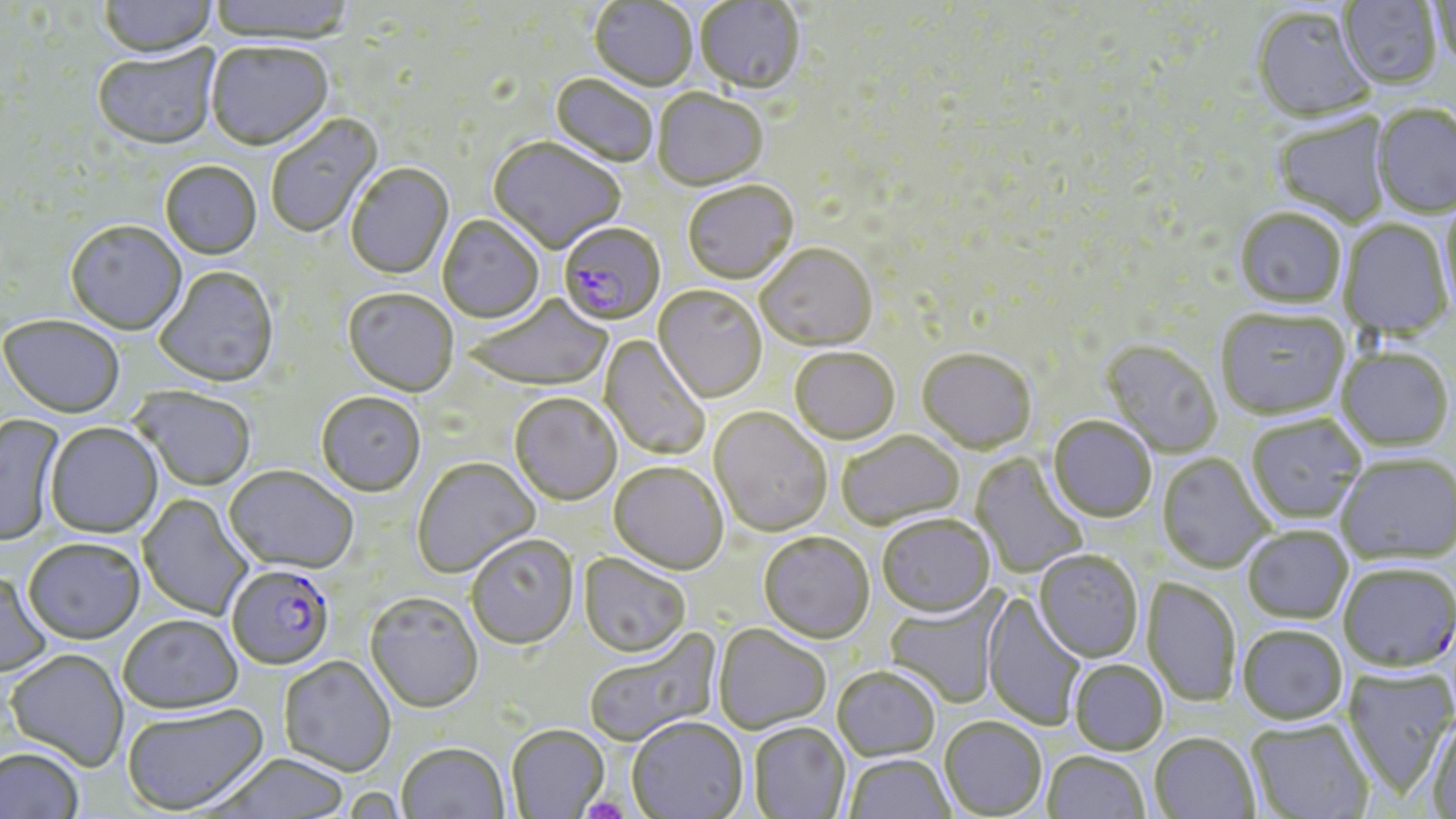
Summary:
  - Coordinate format: approximate bounding boxes as (x1, y1, x2, y2) in pixels
  - Platelet locations: (580, 797, 630, 819)
  - Plasmodium falciparum-infected red blood cell locations: (558, 224, 666, 328), (227, 567, 334, 671)
  - Uninfected red blood cell locations: (97, 0, 218, 61), (209, 0, 355, 46), (1427, 0, 1456, 75), (589, 1, 697, 92), (694, 1, 805, 97), (1338, 1, 1443, 90), (1251, 8, 1375, 125), (206, 44, 333, 153), (92, 46, 221, 152), (549, 75, 658, 169), (653, 91, 769, 192), (1371, 103, 1456, 217), (266, 113, 384, 240), (1272, 113, 1392, 227), (488, 138, 626, 256), (160, 162, 262, 262), (346, 164, 454, 280), (682, 182, 799, 288), (1441, 197, 1456, 318), (1235, 208, 1346, 308), (437, 216, 544, 325), (1339, 220, 1453, 339), (65, 222, 187, 336), (755, 246, 878, 353), (154, 268, 279, 390), (653, 287, 767, 405), (342, 290, 458, 398), (464, 296, 614, 394), (1215, 307, 1350, 419), (0, 318, 125, 420), (599, 333, 711, 460), (1100, 340, 1223, 459), (1337, 347, 1453, 451), (789, 349, 900, 446), (916, 350, 1038, 455), (129, 388, 256, 492), (316, 394, 426, 499), (509, 395, 622, 507), (708, 409, 832, 538), (0, 414, 64, 547), (1246, 414, 1366, 524), (1047, 417, 1157, 523), (45, 424, 164, 539), (837, 432, 965, 531), (971, 453, 1088, 580), (1157, 453, 1274, 574), (1336, 453, 1456, 563), (412, 459, 541, 579), (608, 463, 728, 576), (223, 468, 358, 577), (137, 494, 253, 621), (878, 516, 995, 620), (1243, 525, 1353, 624), (758, 534, 874, 645), (466, 536, 579, 652), (23, 541, 145, 646), (1034, 550, 1143, 662), (578, 554, 690, 660), (1338, 562, 1455, 671), (0, 572, 52, 678), (1142, 576, 1241, 708), (982, 591, 1087, 731), (884, 593, 1005, 708), (365, 595, 483, 715), (117, 617, 244, 717), (712, 625, 830, 735), (1237, 625, 1348, 725), (584, 629, 722, 747), (5, 651, 129, 772), (279, 658, 396, 778), (1069, 661, 1168, 756), (1342, 665, 1456, 800), (832, 669, 940, 763), (122, 704, 269, 817), (1426, 717, 1456, 819), (939, 718, 1047, 818), (1246, 719, 1374, 818), (627, 720, 749, 819), (748, 723, 849, 818), (506, 726, 610, 818), (1149, 733, 1259, 819), (397, 745, 509, 819), (0, 748, 84, 819), (1043, 752, 1150, 819), (210, 754, 351, 818), (844, 755, 956, 819)
  - Slide-level diagnosis: Plasmodium falciparum
  - Magnification: 1000x
  - Modality: optical microscopy
  - Image size: 1456×819 pixels
  - Field of view: one of a larger specimen
  - Preparation: thin blood film
  - Stain: May-Grünwald-Giemsa